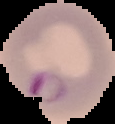

{
  "malaria_status": "parasitized",
  "image_type": "segmented cell region on a black background",
  "preparation": "thin blood smear",
  "image_size": "115×124 pixels"
}